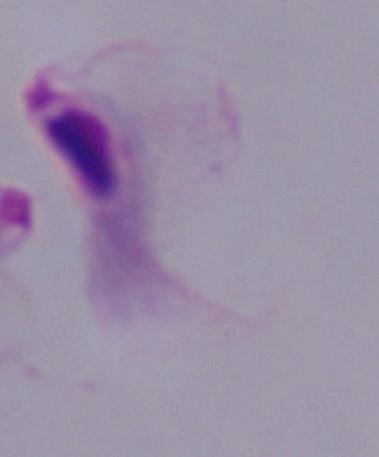
modality = photomicrograph
magnification = 1000x
identification = trichomonad